Classify this cell by malaria status.
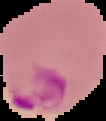

Parasitized.

Summary:
  - Preparation: thin blood smear
  - Image type: segmented cell region on a black background
  - Image size: 106×121 pixels